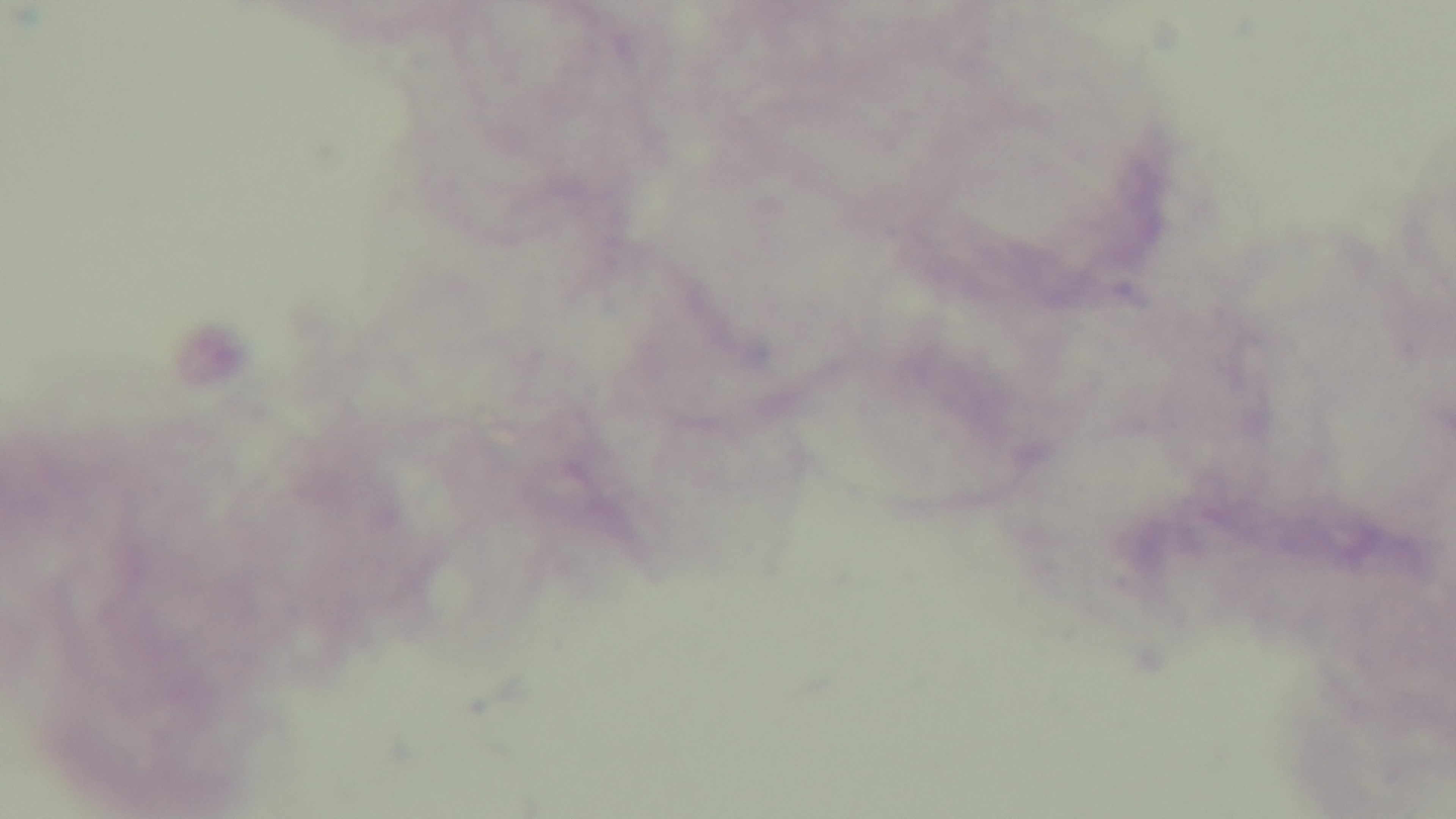

Oil-immersion objective, 100x. Mounted 4K digital camera. Single field of view. Malaria status: negative. Giemsa stain. Light microscopy. Preparation: thick.